Find each parasitized RBC.
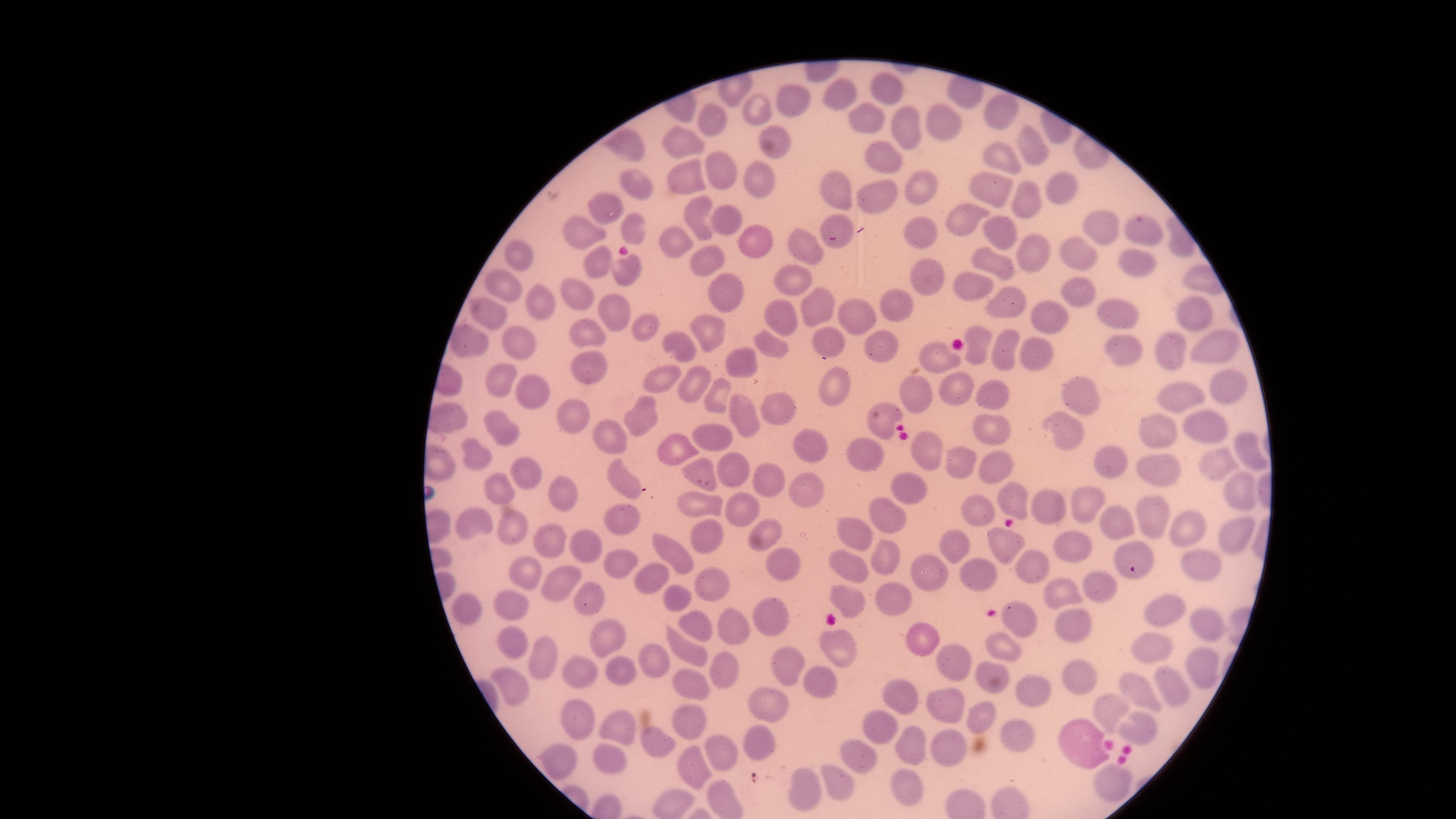
No parasitized RBCs identified.

Approximate marker points as (x, y) in pixels.
Summary:
  - Uninfected RBCs: (893, 82), (840, 97), (782, 101), (1000, 107), (758, 108), (871, 114), (709, 122), (949, 122), (910, 126), (773, 140), (630, 142), (679, 143), (1032, 145), (1003, 155), (875, 157), (679, 170), (718, 171), (757, 178), (833, 183), (638, 185), (986, 189), (920, 190), (1053, 194), (876, 196), (1024, 201), (609, 208), (699, 214), (961, 218), (727, 219), (841, 220), (1107, 222), (918, 229), (1000, 229), (1149, 232), (631, 233), (588, 234), (675, 239), (759, 240), (811, 248), (1038, 249), (521, 252), (597, 257), (1073, 259), (698, 260), (991, 260), (1138, 267), (623, 269), (932, 273), (790, 275), (506, 283), (720, 284), (974, 285), (1075, 285), (580, 294), (1001, 297), (899, 299), (533, 301), (613, 304), (811, 305), (488, 309), (1111, 309), (1051, 312), (857, 313), (779, 317), (1194, 318), (705, 328), (644, 332), (585, 334), (826, 335), (525, 340), (475, 344), (1213, 344), (685, 346), (772, 347), (1166, 347), (979, 348), (1032, 348), (881, 349), (1124, 349), (930, 355), (1003, 356), (739, 365), (585, 366), (658, 374), (953, 377), (696, 378), (501, 383), (1228, 385), (833, 387), (524, 390), (1184, 390), (715, 391), (920, 394), (996, 394), (1080, 396), (775, 408), (643, 413), (576, 415), (878, 416), (749, 420), (503, 422), (1203, 422), (1160, 427), (1063, 430), (991, 432), (615, 433), (717, 433), (919, 442), (810, 443), (677, 445), (1238, 447), (867, 452), (1107, 454), (475, 457), (956, 459), (1215, 461), (996, 462), (1161, 464), (698, 470), (523, 471), (734, 471), (906, 478), (627, 481), (766, 482), (1234, 484), (496, 487), (800, 490), (565, 496), (1012, 496), (1050, 502), (703, 503), (1093, 504), (745, 511), (881, 512), (975, 514), (1158, 517), (621, 518), (474, 520), (511, 522), (1118, 523), (764, 530), (1190, 530), (1237, 531), (545, 535), (855, 535), (998, 535), (703, 541), (580, 547), (1073, 547), (676, 549), (954, 551), (1126, 551), (881, 555), (1200, 560), (1030, 562), (617, 564), (846, 566), (775, 567), (525, 569), (653, 572), (980, 573), (931, 575), (707, 582), (563, 585), (1097, 586), (1066, 593), (896, 594), (681, 597), (581, 599), (855, 599), (478, 605), (514, 605), (1163, 609), (694, 616), (1023, 617), (777, 618), (1072, 621), (730, 625), (1200, 625), (512, 635), (610, 637), (689, 643), (840, 648), (927, 648), (1005, 649), (1153, 649), (541, 658), (648, 661), (954, 663), (785, 664), (723, 668), (620, 669), (1200, 670), (585, 673), (1084, 677), (507, 680), (819, 682), (992, 682), (686, 684), (1170, 684), (1138, 686), (1030, 690), (901, 695), (762, 700), (944, 709), (1107, 709), (982, 717), (576, 719), (687, 722), (1134, 722), (885, 728), (614, 729), (759, 736), (658, 739), (1016, 739), (1078, 741), (906, 746), (943, 746), (726, 750), (608, 754), (864, 758), (562, 759), (697, 769), (841, 778), (1117, 784), (806, 786), (906, 786)
  - Field of view: single
  - Stain: Giemsa
  - Visible region: circular
  - Image size: 1456×819 pixels
  - Preparation: thin blood smear
  - Capture: smartphone photograph through the microscope eyepiece